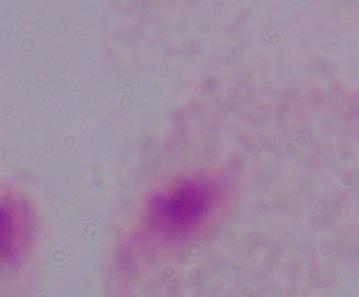

A trichomonad is seen. Photomicrograph. Captured at 1000x magnification.